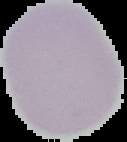 From a thin blood smear. Cell region segmented out of the field of view; the surrounding area is masked to black. Image is 127×142 pixels. Result: negative for malaria parasites.